Locate leukocytes (white blood cells).
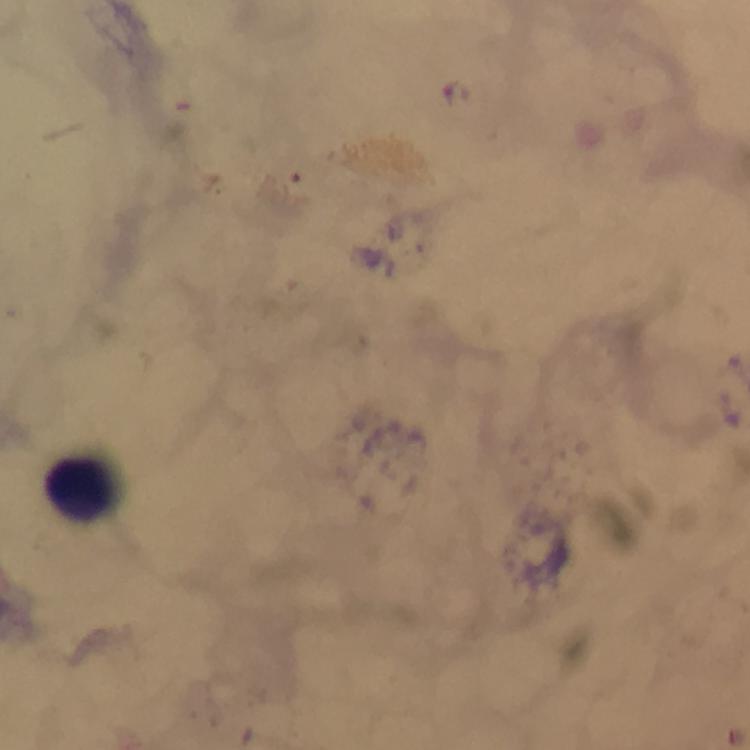

Approximate object centers, in pixels from the top-left corner.
Leukocytes: (x=76, y=485).

stain = Giemsa
image size = 750×750 pixels
preparation = thick smear
cropped from = a single field of view
capture = smartphone camera through the microscope
malaria parasites = none detected
magnification = 100x
context = from a diagnostic examination for malaria
immersion oil = used